State which parasite is depicted.
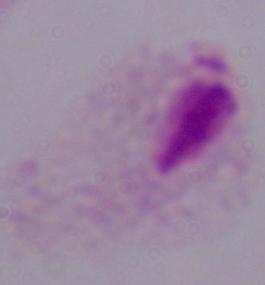

A trichomonad.

Summary:
  - Magnification: 1000x
  - Modality: micrograph